Classify this cell by malaria status.
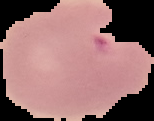

It is parasitized.

Summary:
  - Image size: 154×121 pixels
  - Image type: segmented cell region with the area outside set to black
  - Preparation: thin blood smear